Comment on the morphology of the erythrocytes.
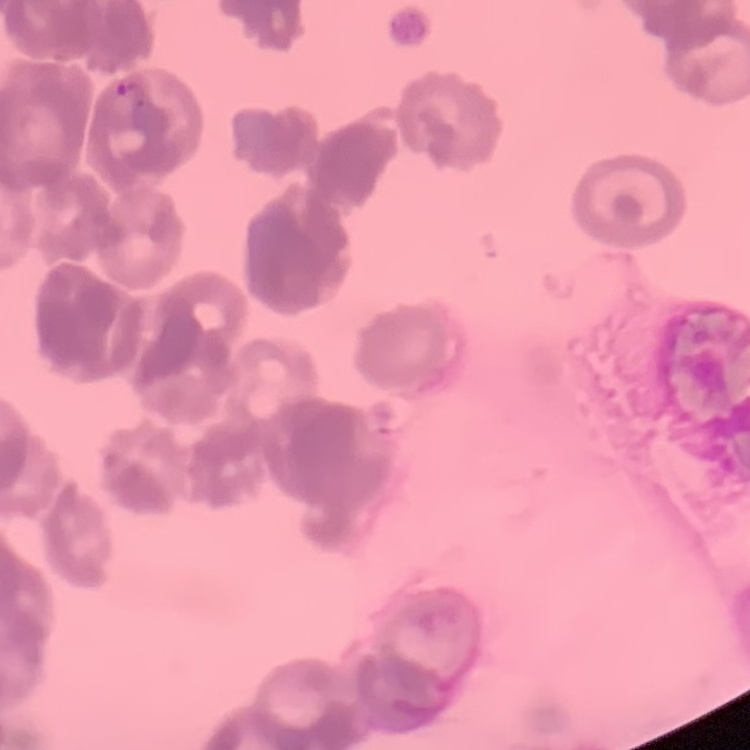
They show rouleaux formation.

preparation = thin blood smear
stain = Field's or Giemsa
image type = one tile cut from a larger photomicrograph